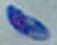
identification = Toxoplasma gondii
magnification = 1000x
modality = micrograph